State the blood parasite species.
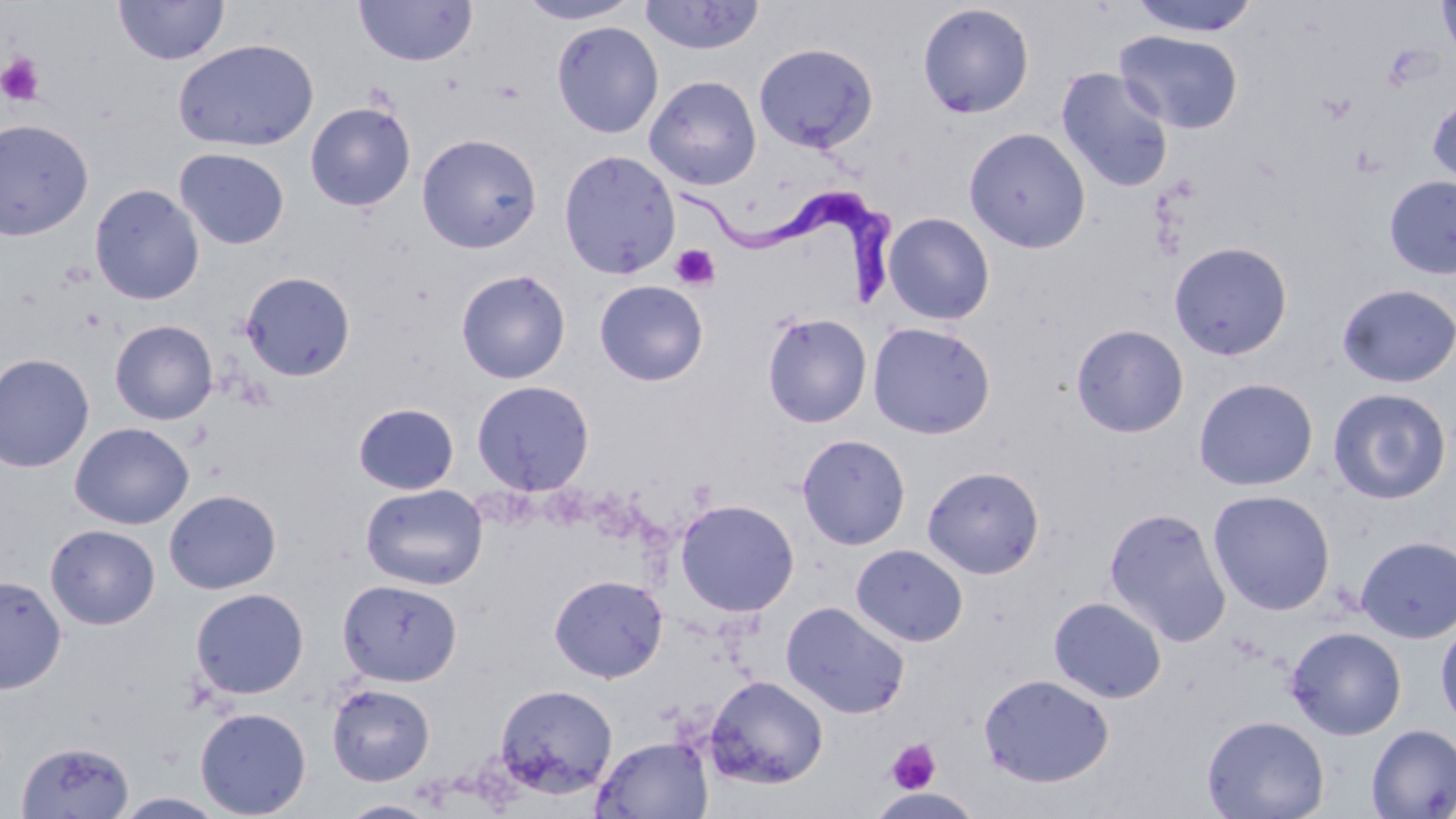

Trypanosoma brucei.

image size = 1456×819 pixels
stain = May-Grünwald-Giemsa
magnification = 1000x
uninfected red blood cell locations = approximate bounding boxes as [x1, y1, x2, y2] in pixels: [354, 0, 477, 67], [516, 0, 642, 24], [1128, 0, 1262, 37], [1437, 0, 1456, 59], [114, 1, 230, 65], [638, 1, 765, 55], [917, 3, 1035, 118], [550, 20, 664, 138], [1115, 30, 1244, 134], [173, 39, 319, 152], [753, 42, 878, 154], [1056, 67, 1175, 193], [644, 75, 762, 190], [1427, 95, 1456, 189], [305, 101, 416, 212], [0, 118, 94, 240], [964, 127, 1091, 253], [416, 132, 542, 253], [174, 148, 290, 250], [558, 149, 681, 280], [1383, 176, 1456, 279], [89, 184, 204, 305], [883, 212, 995, 325], [1169, 241, 1293, 361], [456, 269, 571, 383], [241, 271, 355, 381], [594, 280, 708, 386], [1336, 283, 1456, 387], [761, 312, 872, 429], [109, 320, 218, 425], [867, 322, 996, 439], [1070, 323, 1189, 438], [0, 353, 95, 472], [1193, 377, 1319, 491], [471, 379, 595, 496], [1327, 387, 1452, 505], [352, 402, 459, 495], [69, 422, 194, 529], [796, 433, 911, 550], [922, 465, 1045, 579], [360, 484, 488, 590], [163, 488, 282, 595], [1208, 489, 1336, 616], [675, 498, 800, 617], [1103, 506, 1232, 647], [45, 524, 160, 630], [1356, 536, 1456, 643], [850, 544, 968, 647], [0, 574, 67, 694], [549, 574, 668, 682], [336, 578, 462, 687], [190, 587, 309, 699], [1048, 597, 1167, 703], [781, 600, 910, 719], [1435, 619, 1456, 732], [1286, 626, 1407, 740], [979, 673, 1114, 788], [705, 675, 829, 789], [326, 683, 435, 786], [494, 684, 618, 798], [194, 706, 312, 818], [1201, 714, 1329, 819], [1365, 723, 1456, 818], [592, 735, 714, 818], [15, 740, 135, 818], [115, 792, 228, 818], [338, 799, 441, 818]
field of view = single
platelet locations = approximate bounding boxes as [x1, y1, x2, y2] in pixels: [0, 53, 46, 107], [1317, 91, 1357, 126], [670, 244, 721, 291], [886, 739, 941, 794]
Trypanosoma brucei locations = approximate bounding boxes as [x1, y1, x2, y2] in pixels: [682, 184, 900, 314]
preparation = thin blood film
modality = light microscopy